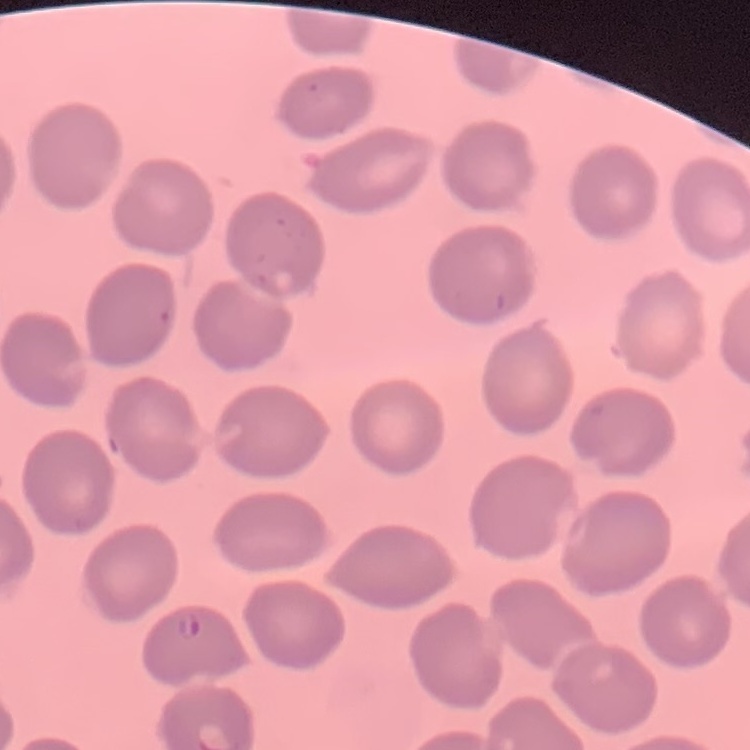 The erythrocytes show no rouleaux formation. Thin blood film. Field's or Giemsa stain. Square crop of a larger photomicrograph.